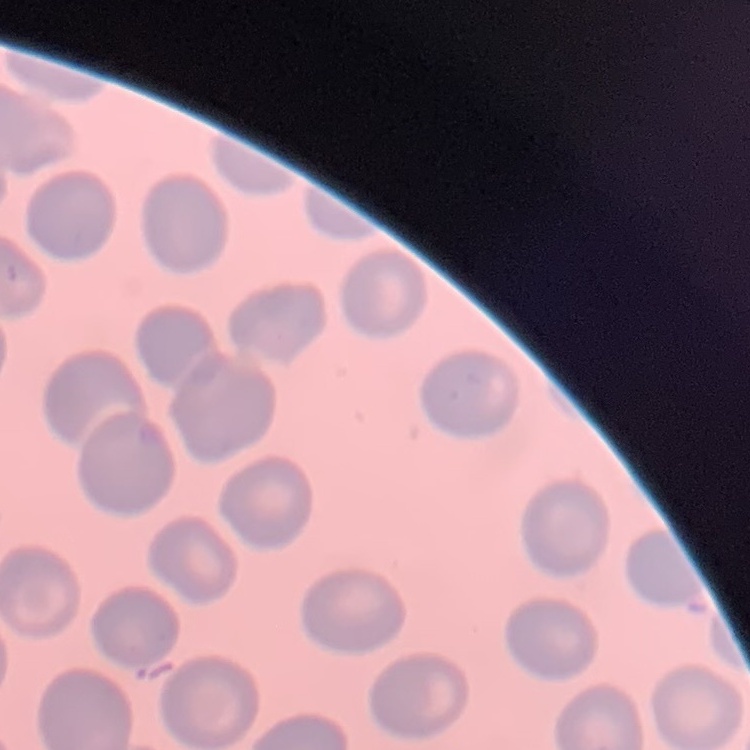

Summary:
  - Red blood cell morphology: no rouleaux formation
  - Image type: square crop of a larger photomicrograph
  - Preparation: thin blood smear
  - Stain: Field's or Giemsa